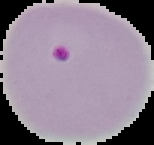 Image is 154×145 pixels. From a thin blood smear. Result: malaria parasites detected. The area outside the segmented cell region is set to black.